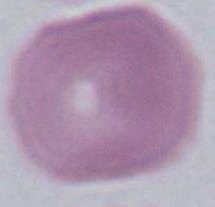
1000x magnification. A red blood cell is seen. Micrograph.